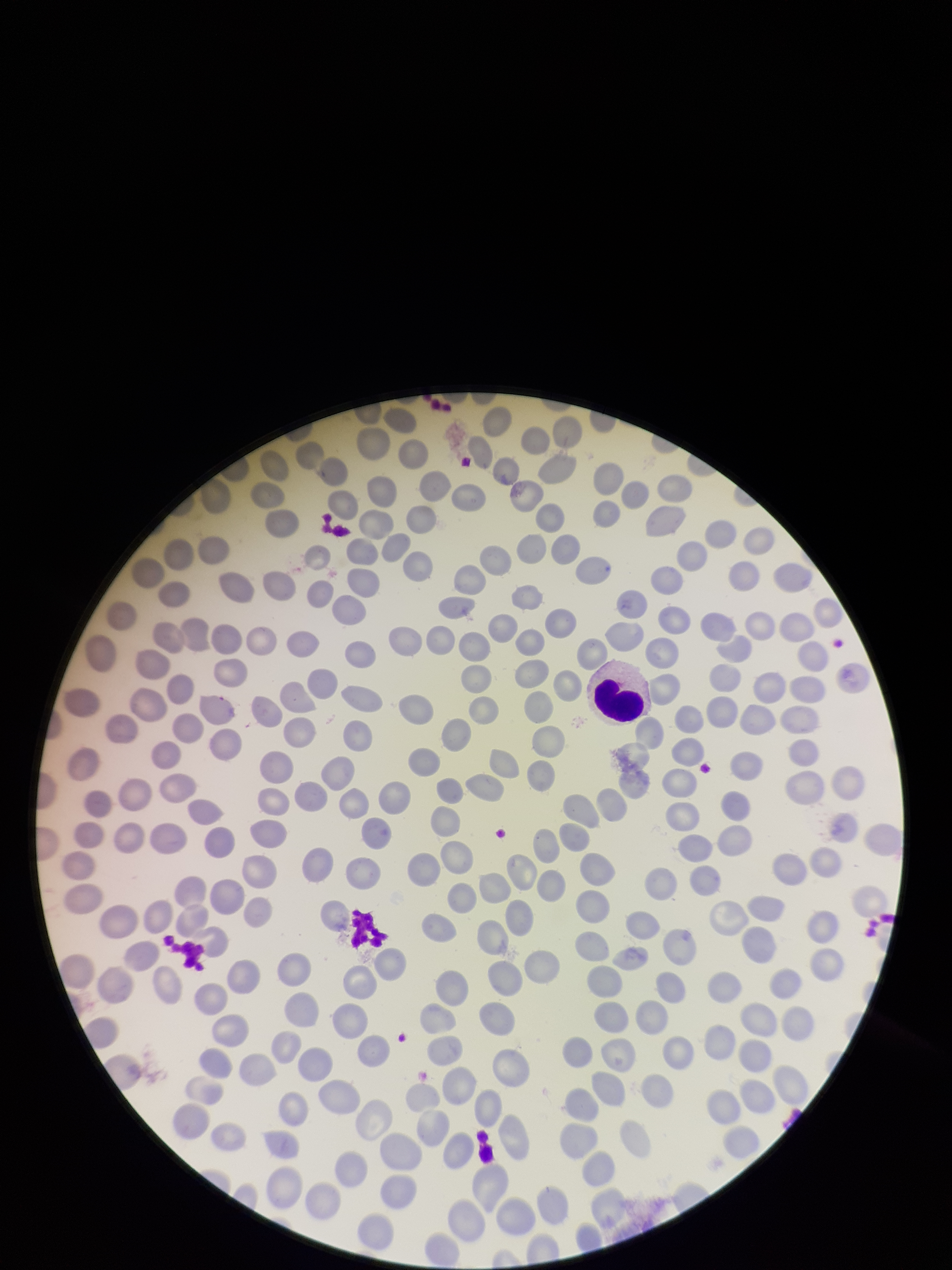 Red blood cell count: 266. Photographed through the microscope eyepiece with a smartphone camera. Image is 952×1270 pixels. Preparation: thin blood smear. Single field of view. Giemsa stain. Parasitized red blood cells: none seen. Parasitized red blood cell count: 0. Patient malaria status: negative.